Assess this cell for malaria.
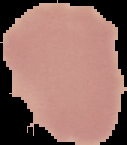

Uninfected.

Image is 127×145 pixels. From a thin blood film. Cell region segmented out of the field of view; the surrounding area is masked to black.